State which cell type is depicted.
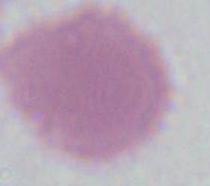

This is an erythrocyte.

Micrograph. Captured at 1000x magnification.